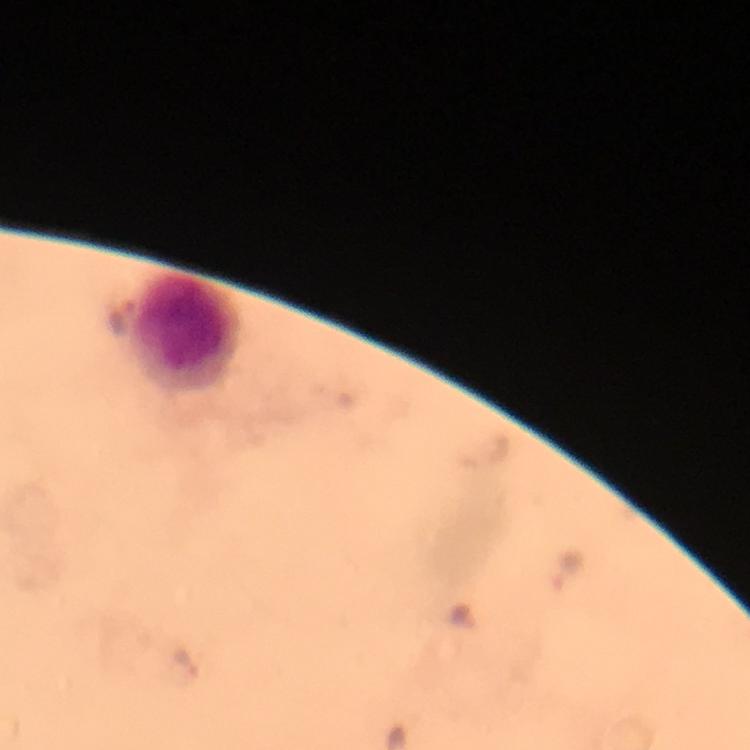

Approximate centers as [x, y] in pixels.
Summary:
  - Leukocyte locations: [189, 331]
  - Plasmodium parasite locations: [567, 568], [182, 662]
  - Immersion oil: applied
  - Context: from a malaria diagnostic workup
  - Stain: Giemsa
  - Capture: smartphone photograph through a microscope
  - Image size: 750×750 pixels
  - Cropped from: one field of view
  - Magnification: 100x
  - Preparation: thick blood smear